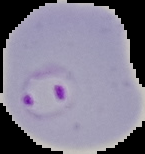

{
  "preparation": "thin blood film",
  "malaria_status": "parasitized",
  "image_type": "segmented cell region on a black background",
  "image_size": "145×154 pixels"
}